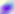

modality = micrograph
magnification = 400x
identification = Toxoplasma gondii